Locate every malaria parasite by life-cycle stage, and every leukocyte.
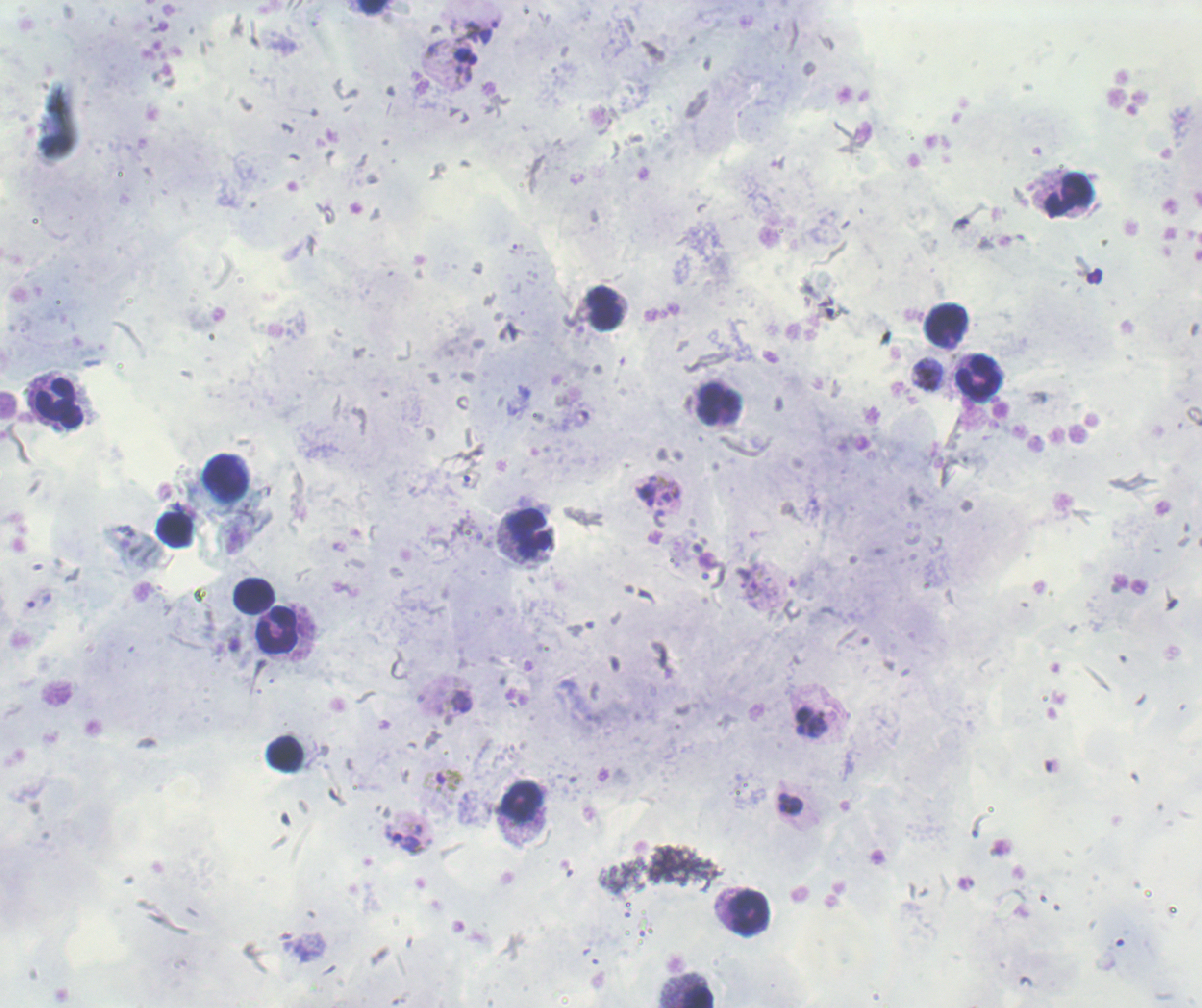
Approximate centers as (x, y) in pixels.
Trophozoites: (926, 373), (646, 495), (39, 599), (803, 720), (818, 727), (790, 798), (789, 808), (402, 838).
Gametocytes: (441, 781).
No schizont forms observed.
Leukocytes: (1068, 194), (604, 308), (947, 326), (979, 377), (718, 402), (58, 404), (225, 477), (175, 532), (528, 532), (254, 596), (274, 632), (286, 754), (520, 802), (749, 912), (699, 996).

Summary:
  - Background quality: good
  - Magnification: 100x
  - Image size: 1202×1008 pixels
  - Preparation: thick blood film
  - Stain: Romanowsky
  - Field of view: single
  - Context: previously used in a real diagnosis